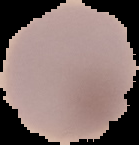 Cell region segmented out of the field of view; the surrounding area is masked to black. Malaria status: uninfected. Image is 139×145 pixels. From a thin blood film.